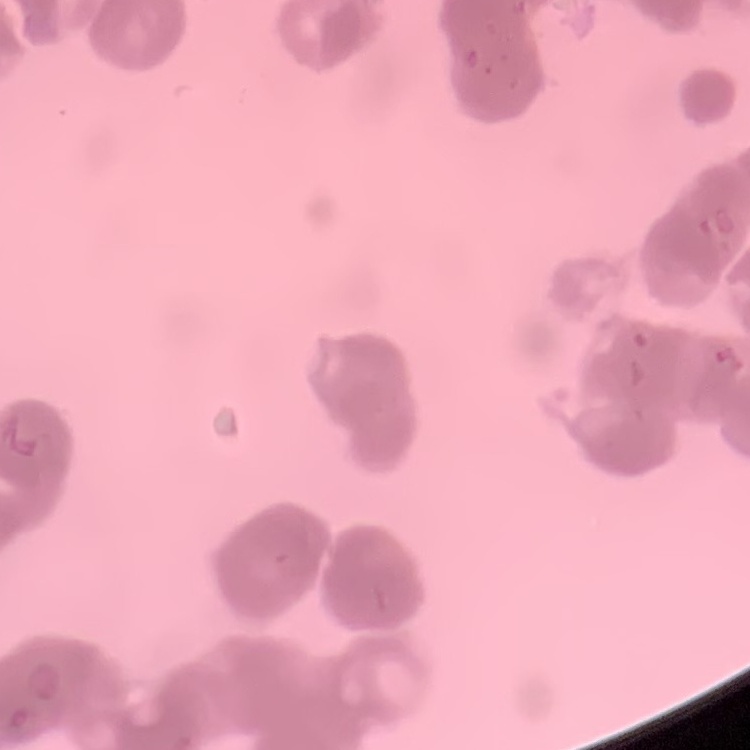
Summary:
  - Erythrocyte morphology: rouleaux formation
  - Image type: square crop of a larger photomicrograph
  - Preparation: thin peripheral smear
  - Stain: Field's or Giemsa